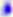

Summary:
  - Magnification: 400x
  - Identification: Toxoplasma gondii
  - Modality: micrograph